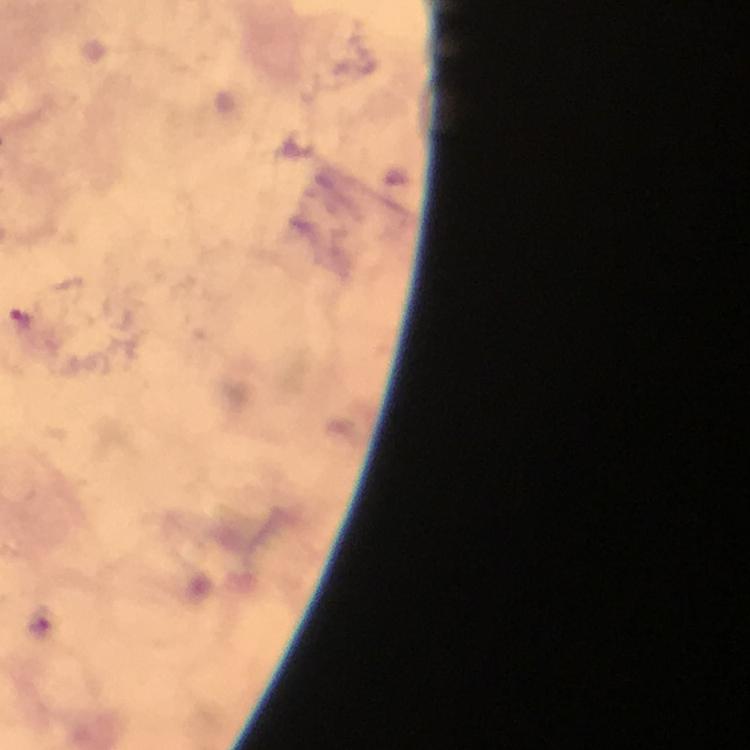

context: from a diagnostic examination for malaria
image_size: 750×750 pixels
malaria_parasite_locations: 'approximate centers as {x, y} in pixels: {20, 318}'
capture: smartphone photograph through a microscope
preparation: thick blood film
cropped_from: one field of view
stain: Giemsa
immersion_oil: applied
magnification: 100x